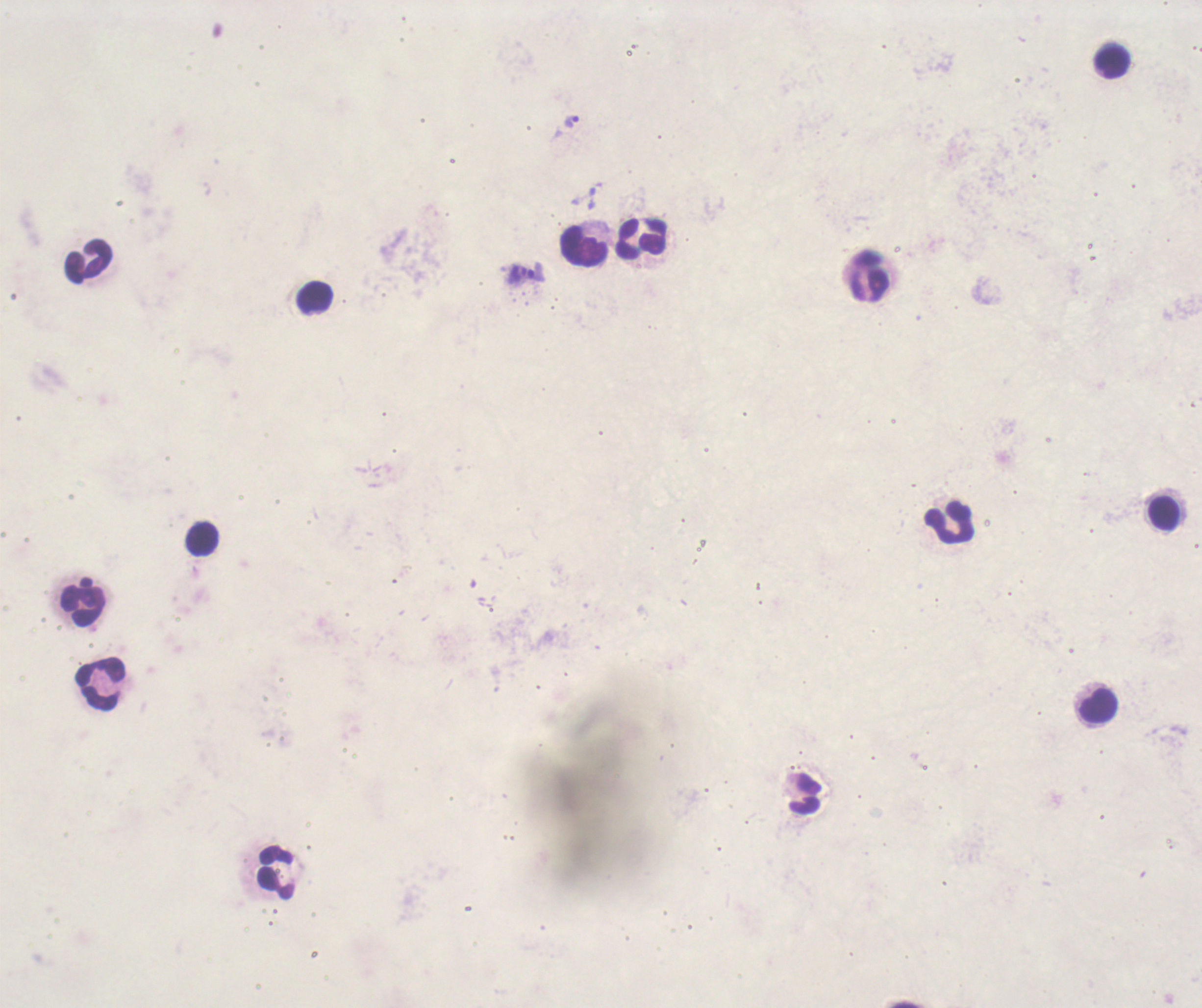 Approximate centers as {x, y} in pixels. Trophozoite locations: {574, 122}, {526, 272}. Leukocyte locations: {1113, 62}, {640, 238}, {585, 246}, {89, 260}, {868, 278}, {315, 298}, {1163, 513}, {951, 522}, {203, 540}, {84, 601}, {99, 683}, {1097, 706}, {277, 873}. Result: malaria parasites identified. Romanowsky-stained preparation. Thick blood smear. Background quality: poor. 100x magnification. Single field of view. Coloration quality: bad. Previously used in a real diagnosis. Image is 1202×1008 pixels.